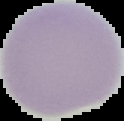

{
  "result": "no malaria parasites seen",
  "preparation": "thin blood film",
  "image_type": "segmented cell region on a black background",
  "image_size": "124×121 pixels"
}